Point out each leukocyte.
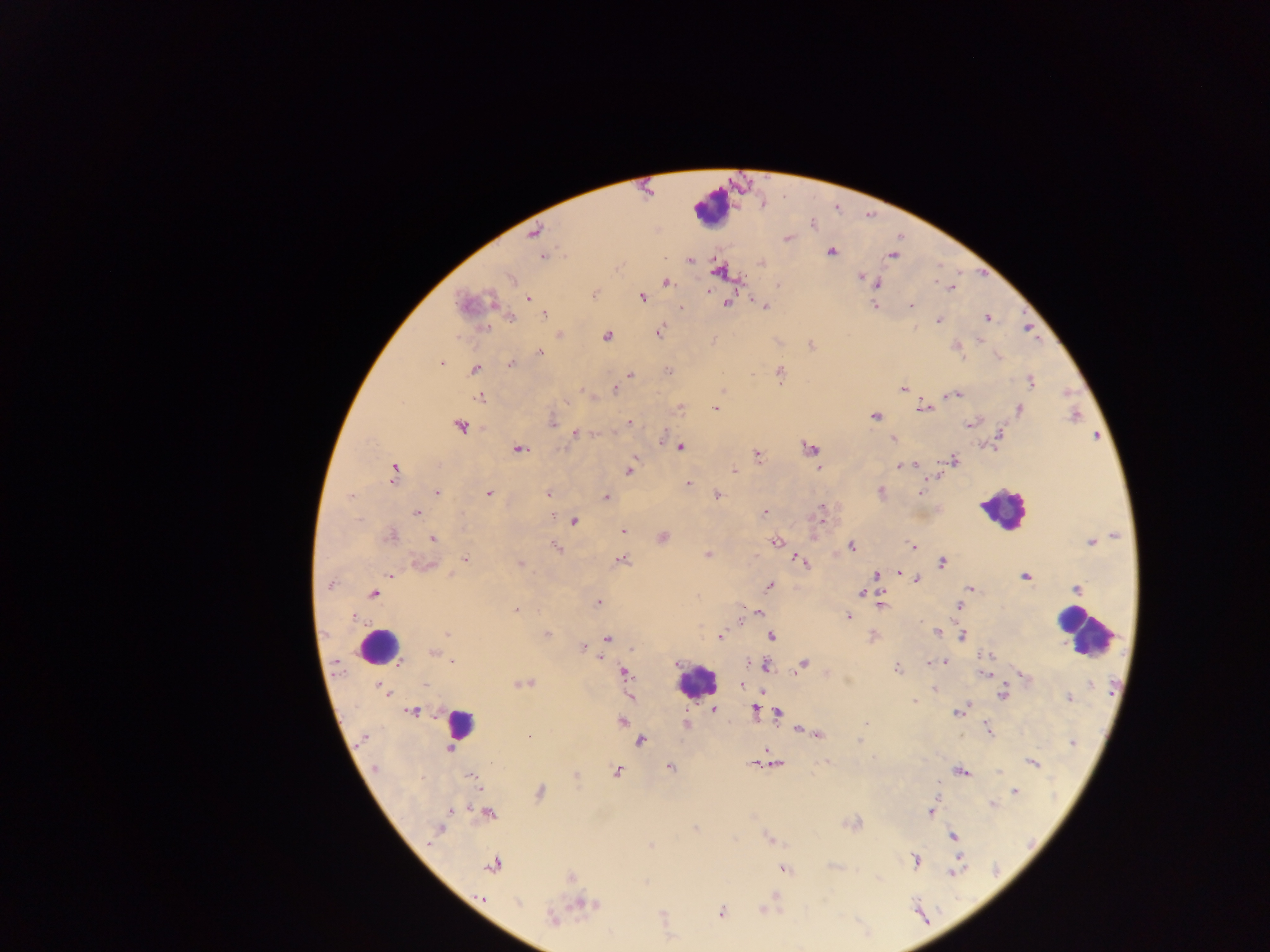
Approximate centers as [x, y] in pixels.
Leukocytes: [711, 208], [1002, 509], [1083, 631], [379, 647], [696, 680], [458, 725].

Summary:
  - Plasmodium parasite locations: [812, 223], [534, 232], [787, 238], [831, 253], [543, 256], [892, 256], [690, 260], [761, 262], [718, 271], [862, 277], [510, 279], [870, 280], [666, 283], [876, 283], [951, 287], [594, 294], [642, 296], [527, 299], [467, 304], [726, 304], [875, 305], [765, 306], [912, 306], [681, 308], [544, 316], [511, 318], [987, 318], [938, 320], [659, 332], [559, 335], [606, 336], [811, 345], [957, 347], [540, 353], [999, 357], [441, 363], [510, 365], [474, 368], [667, 371], [631, 374], [780, 374], [1031, 382], [902, 388], [614, 389], [582, 391], [951, 395], [479, 398], [566, 402], [679, 408], [716, 408], [922, 408], [1019, 409], [875, 417], [629, 422], [553, 423], [970, 424], [460, 427], [577, 433], [999, 436], [892, 439], [680, 447], [810, 448], [519, 449], [757, 455], [954, 461], [914, 465], [900, 466], [817, 468], [629, 470], [734, 470], [394, 472], [688, 483], [880, 491], [437, 492], [489, 493], [548, 493], [920, 493], [717, 495], [606, 498], [416, 513], [763, 513], [821, 515], [574, 522], [622, 532], [390, 536], [663, 538], [433, 539], [1091, 541], [776, 542], [851, 546], [556, 547], [913, 547], [707, 555], [466, 559], [621, 560], [801, 561], [942, 562], [424, 563], [521, 564], [899, 572], [876, 574], [391, 576], [1025, 577], [916, 579], [330, 585], [769, 586], [969, 589], [1076, 589], [861, 593], [374, 594], [598, 603], [881, 604], [959, 605], [516, 610], [758, 612], [354, 616], [848, 617], [938, 632], [447, 634], [547, 634], [720, 635], [872, 636], [772, 637], [962, 637], [607, 638], [582, 647], [433, 653], [453, 660], [943, 661], [677, 663], [932, 663], [804, 664], [765, 666], [897, 668], [625, 674], [984, 674], [1024, 676], [523, 683], [1090, 684], [425, 685], [742, 685], [382, 688], [934, 688], [385, 692], [1002, 695], [1069, 698], [915, 701], [713, 709], [755, 709], [412, 711], [958, 712], [778, 713], [622, 720], [866, 722], [686, 724], [989, 729], [800, 730], [808, 732], [817, 734], [530, 737], [364, 738], [860, 740], [640, 741], [1072, 743], [450, 749], [827, 762], [753, 763], [1033, 763], [776, 764], [670, 767], [375, 768], [617, 771], [961, 771], [576, 776], [472, 777], [1014, 792], [540, 793], [992, 804], [931, 810], [453, 811], [489, 813], [851, 824], [695, 827], [439, 829], [953, 836], [769, 839], [651, 846], [915, 861], [493, 866], [833, 866], [784, 870], [955, 872], [571, 877], [774, 895], [481, 896], [518, 903], [583, 905], [720, 912], [662, 915], [551, 918]
  - Image size: 1270×952 pixels
  - Country: Ghana
  - Field of view: single
  - Capture: mobile-phone photograph through a microscope
  - Preparation: thick blood film